Report the malaria status of this cell.
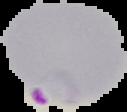
It is parasitized.

Summary:
  - Image size: 127×112 pixels
  - Image type: segmented cell region with the area outside set to black
  - Preparation: thin blood film